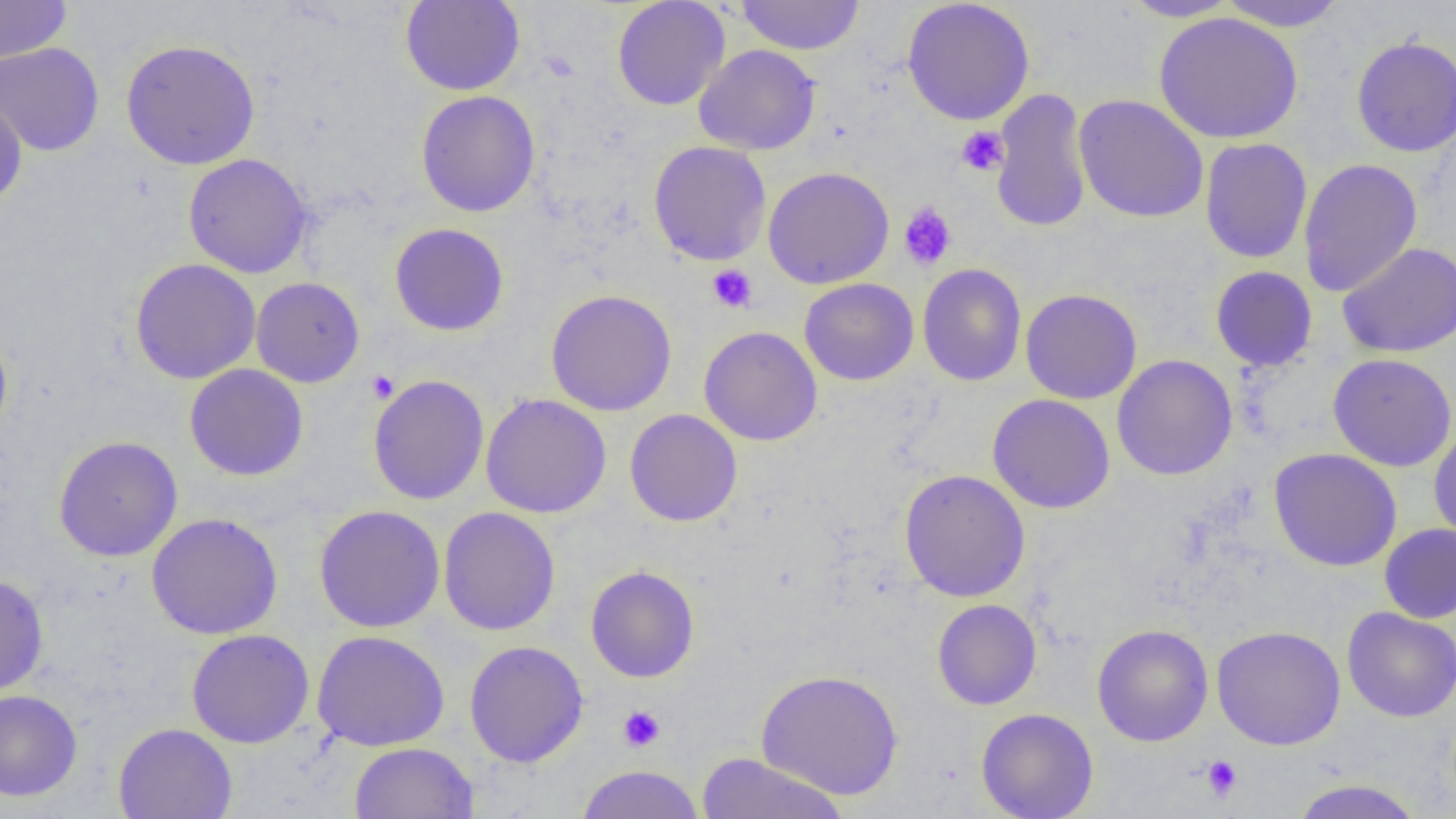
Approximate bounding boxes as (x1, y1, x2, y2) in pixels. Uninfected red blood cell locations: (0, 0, 72, 64), (400, 0, 525, 96), (612, 0, 730, 111), (736, 0, 864, 55), (902, 0, 1035, 126), (1119, 0, 1242, 22), (1216, 0, 1346, 31), (1153, 11, 1304, 144), (1351, 35, 1456, 157), (120, 39, 260, 170), (0, 42, 105, 156), (694, 44, 821, 155), (990, 87, 1093, 233), (415, 90, 540, 217), (0, 92, 28, 210), (1073, 94, 1209, 223), (1199, 137, 1313, 264), (648, 140, 771, 266), (183, 153, 314, 278), (1298, 158, 1423, 297), (763, 166, 894, 289), (390, 223, 509, 336), (1337, 242, 1456, 358), (130, 258, 261, 384), (917, 264, 1027, 386), (1210, 266, 1318, 371), (251, 276, 365, 388), (799, 278, 919, 385), (1020, 288, 1143, 404), (546, 289, 677, 416), (698, 326, 823, 446), (0, 329, 12, 442), (1327, 353, 1456, 471), (1112, 355, 1238, 480), (184, 364, 309, 481), (368, 374, 489, 505), (480, 393, 612, 518), (987, 394, 1115, 514), (624, 409, 742, 527), (1428, 425, 1456, 545), (53, 435, 183, 562), (1269, 448, 1402, 572), (898, 468, 1031, 603), (314, 504, 445, 633), (438, 506, 561, 636), (146, 512, 284, 639), (1379, 523, 1456, 623), (586, 565, 700, 683), (0, 574, 49, 697), (932, 599, 1042, 710), (1342, 606, 1456, 722), (1092, 623, 1213, 746), (1211, 625, 1346, 750), (186, 629, 315, 748), (311, 630, 450, 752), (464, 640, 588, 767), (756, 668, 904, 800), (0, 689, 83, 801), (976, 707, 1099, 819), (113, 723, 237, 819), (349, 741, 479, 819), (695, 752, 851, 818), (575, 765, 705, 819), (1288, 779, 1425, 819). Platelet locations: (956, 126, 1009, 176), (898, 202, 957, 271), (707, 264, 757, 313), (366, 370, 399, 403), (617, 705, 665, 753), (1200, 754, 1243, 802). Slide-level diagnosis: no evidence of blood parasites. Light microscopy. Thin blood smear. 1000x magnification. Image is 1456×819 pixels. One field of a larger specimen.